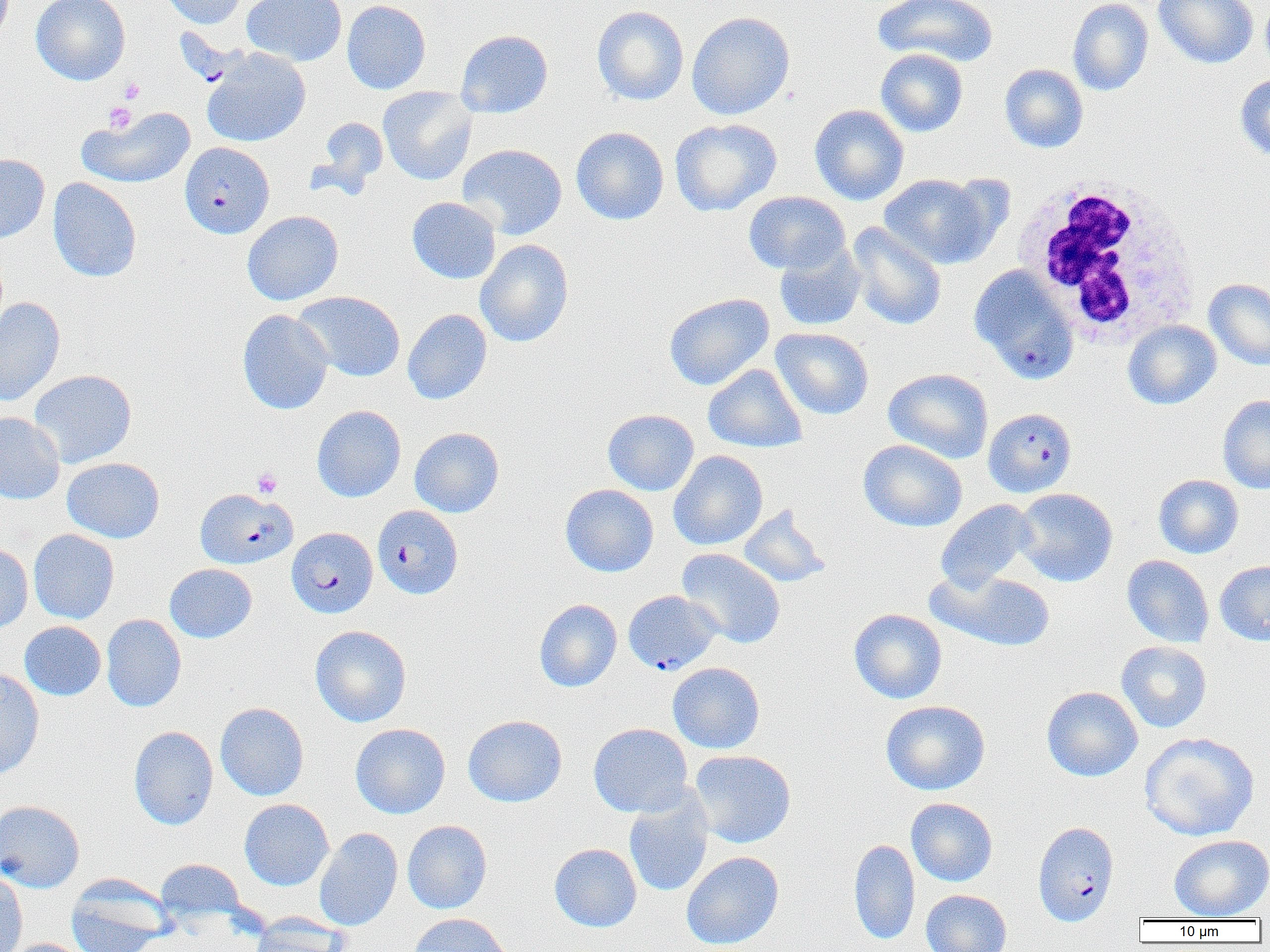

Summary:
  - Coordinate format: approximate bounding boxes as (x1, y1, x2, y2) in pixels
  - White blood cell locations: (1010, 176, 1201, 345)
  - Platelet locations: (120, 78, 145, 103), (104, 102, 137, 133), (252, 468, 282, 498)
  - Plasmodium falciparum-infected red blood cell locations: (179, 142, 274, 239), (969, 265, 1079, 383), (983, 407, 1077, 497), (194, 487, 297, 570), (372, 505, 463, 599), (287, 527, 378, 618), (623, 590, 721, 675), (1032, 820, 1119, 926)
  - Uninfected red blood cell locations: (31, 0, 130, 85), (160, 0, 248, 29), (242, 0, 347, 66), (342, 0, 431, 94), (873, 0, 998, 68), (1067, 0, 1153, 95), (1153, 0, 1259, 69), (1260, 0, 1270, 78), (591, 5, 689, 106), (686, 11, 795, 120), (455, 29, 554, 119), (202, 47, 311, 147), (875, 48, 968, 137), (999, 64, 1088, 153), (1234, 74, 1270, 161), (378, 87, 477, 186), (809, 104, 909, 205), (77, 106, 196, 189), (315, 116, 388, 194), (670, 118, 782, 216), (570, 126, 669, 225), (457, 143, 567, 240), (0, 154, 50, 243), (878, 173, 998, 268), (48, 178, 142, 282), (743, 191, 850, 275), (407, 197, 501, 284), (242, 210, 343, 306), (846, 222, 946, 331), (474, 239, 573, 347), (774, 243, 865, 332), (1204, 278, 1270, 371), (293, 291, 405, 382), (663, 293, 774, 391), (0, 296, 66, 406), (402, 308, 492, 404), (237, 309, 333, 415), (1122, 320, 1221, 410), (771, 327, 874, 420), (703, 363, 807, 453), (883, 368, 994, 464), (29, 369, 137, 467), (1217, 394, 1270, 494), (312, 405, 406, 502), (602, 409, 699, 496), (0, 412, 65, 504), (410, 427, 504, 517), (858, 439, 967, 532), (669, 450, 768, 550), (62, 457, 165, 543), (1153, 474, 1244, 559), (560, 484, 659, 577), (1013, 488, 1118, 586), (935, 500, 1039, 593), (738, 504, 832, 587), (28, 529, 119, 624), (0, 543, 33, 635), (676, 548, 786, 648), (1122, 555, 1214, 648), (1215, 560, 1270, 645), (164, 563, 257, 643), (926, 569, 1057, 652), (534, 598, 622, 692), (848, 608, 947, 704), (101, 614, 186, 712), (19, 621, 106, 700), (310, 625, 412, 727), (1116, 641, 1212, 733), (668, 662, 765, 753), (0, 667, 45, 781), (1041, 686, 1143, 781), (880, 700, 990, 795), (215, 702, 309, 801), (463, 715, 567, 807), (350, 723, 450, 818), (589, 723, 693, 817), (129, 726, 219, 830), (1139, 731, 1259, 841), (690, 749, 796, 848), (624, 787, 714, 897), (239, 798, 334, 891), (906, 798, 998, 886), (0, 800, 84, 893), (402, 820, 492, 914), (314, 827, 403, 931), (1168, 834, 1270, 920), (849, 839, 920, 946), (549, 843, 642, 932), (681, 851, 784, 950), (155, 858, 245, 925), (0, 869, 28, 952), (66, 874, 174, 952), (921, 889, 1011, 952), (407, 913, 513, 952), (250, 914, 349, 952), (6, 938, 93, 952)
  - Slide-level diagnosis: Plasmodium falciparum
  - Magnification: 1000x
  - Image size: 1270×952 pixels
  - Modality: light microscopy
  - Field of view: one of a larger specimen
  - Preparation: thin blood smear